Look for parasitized red blood cells.
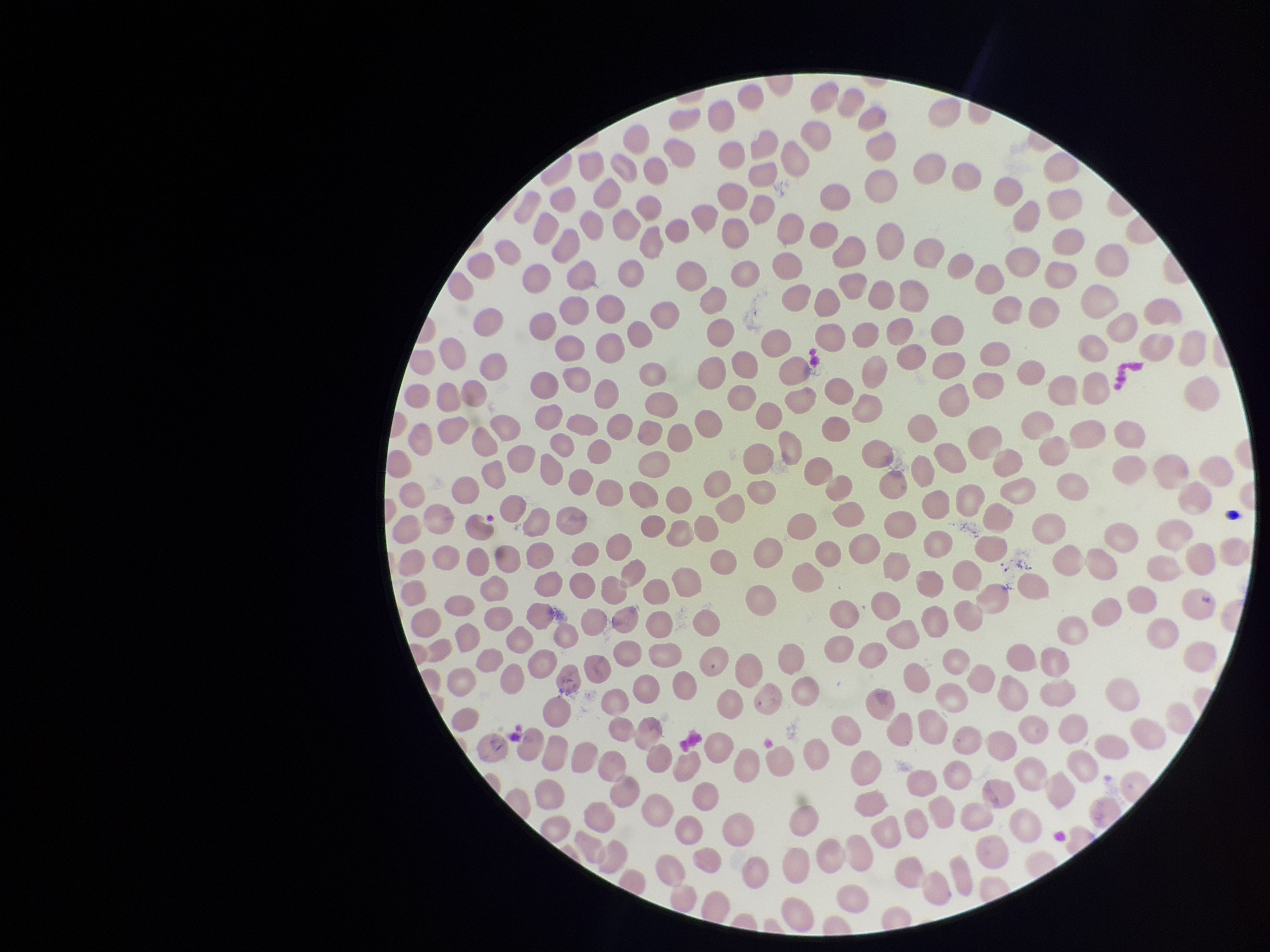

None seen.

Summary:
  - Image size: 1270×952 pixels
  - Capture: smartphone photograph through the microscope eyepiece
  - Parasitized red blood cell count: 0
  - Red blood cell count: 318
  - Patient malaria status: negative
  - Stain: Giemsa
  - Field of view: single
  - Preparation: thin smear